Outline each blood parasite and name the species.
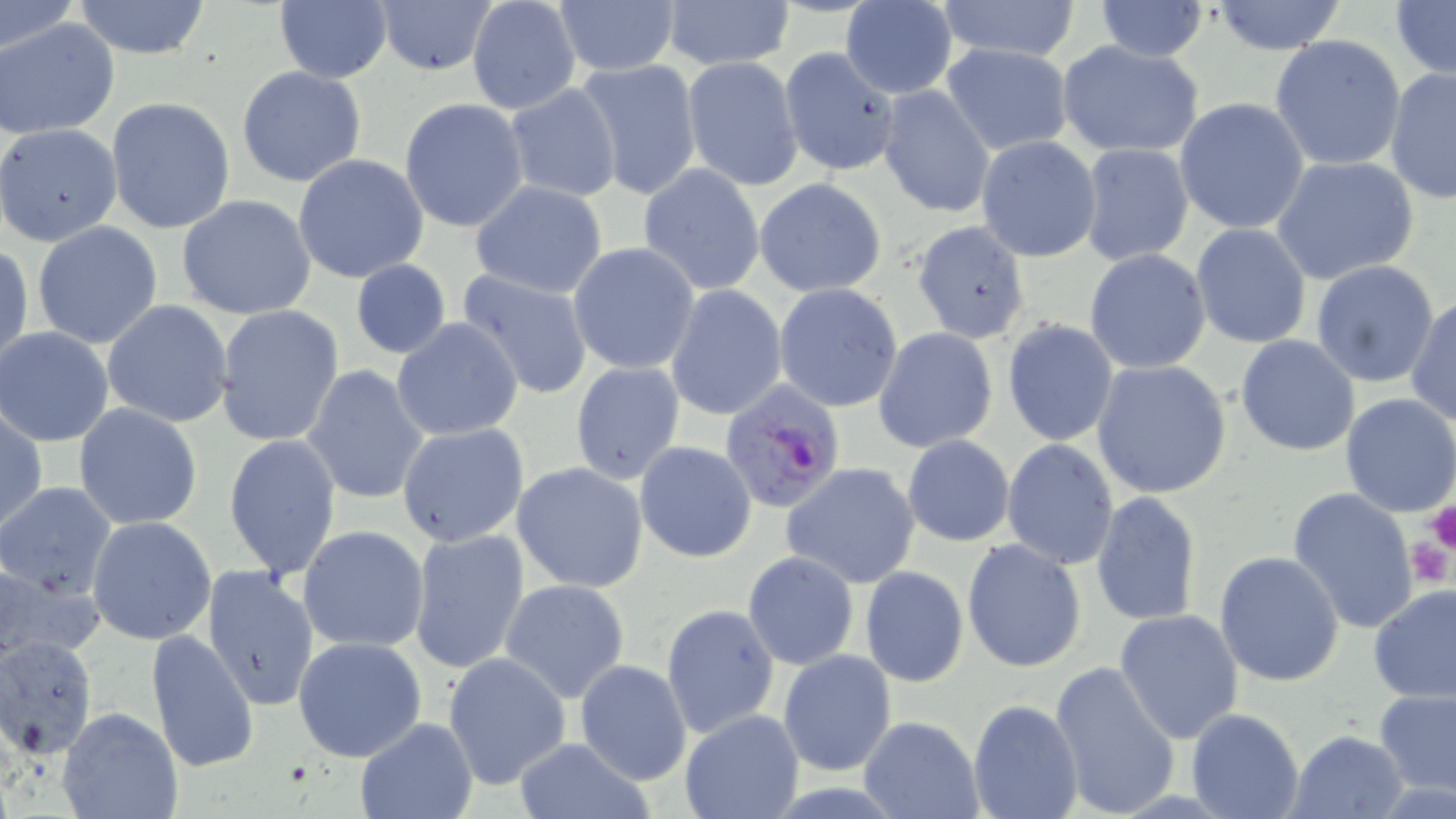
Approximate bounding boxes as named x1/y1/x2/y2 corners in pixels.
Plasmodium falciparum-infected red blood cells: (x1=718, y1=382, x2=846, y2=515).
No Plasmodium ovale, Plasmodium malariae, Plasmodium vivax, Babesia divergens, or Trypanosoma brucei observed.

Uninfected red blood cell locations: (x1=0, y1=0, x2=77, y2=57), (x1=70, y1=0, x2=214, y2=59), (x1=374, y1=0, x2=498, y2=75), (x1=466, y1=0, x2=582, y2=116), (x1=1093, y1=0, x2=1211, y2=62), (x1=273, y1=1, x2=392, y2=84), (x1=550, y1=1, x2=681, y2=76), (x1=658, y1=1, x2=797, y2=71), (x1=840, y1=1, x2=958, y2=98), (x1=933, y1=1, x2=1086, y2=65), (x1=1208, y1=1, x2=1349, y2=54), (x1=1391, y1=2, x2=1455, y2=82), (x1=2, y1=18, x2=121, y2=139), (x1=1269, y1=35, x2=1408, y2=173), (x1=1057, y1=41, x2=1205, y2=158), (x1=941, y1=43, x2=1074, y2=155), (x1=777, y1=46, x2=902, y2=177), (x1=681, y1=57, x2=804, y2=192), (x1=575, y1=58, x2=703, y2=200), (x1=236, y1=65, x2=367, y2=187), (x1=1384, y1=66, x2=1456, y2=203), (x1=504, y1=84, x2=623, y2=202), (x1=876, y1=86, x2=996, y2=218), (x1=106, y1=97, x2=236, y2=234), (x1=400, y1=97, x2=529, y2=233), (x1=1174, y1=97, x2=1310, y2=235), (x1=1, y1=125, x2=123, y2=247), (x1=976, y1=136, x2=1103, y2=262), (x1=1078, y1=143, x2=1196, y2=266), (x1=293, y1=154, x2=430, y2=284), (x1=1272, y1=156, x2=1421, y2=287), (x1=638, y1=164, x2=767, y2=294), (x1=754, y1=178, x2=888, y2=297), (x1=470, y1=181, x2=607, y2=298), (x1=176, y1=195, x2=318, y2=320), (x1=911, y1=219, x2=1031, y2=345), (x1=32, y1=222, x2=164, y2=350), (x1=1189, y1=223, x2=1313, y2=349), (x1=1, y1=241, x2=31, y2=372), (x1=569, y1=242, x2=700, y2=375), (x1=1085, y1=249, x2=1213, y2=374), (x1=349, y1=260, x2=451, y2=359), (x1=1311, y1=261, x2=1440, y2=387), (x1=457, y1=270, x2=594, y2=400), (x1=773, y1=283, x2=904, y2=413), (x1=663, y1=285, x2=789, y2=421), (x1=1406, y1=295, x2=1455, y2=427), (x1=102, y1=299, x2=235, y2=428), (x1=214, y1=304, x2=345, y2=448), (x1=391, y1=318, x2=523, y2=441), (x1=1002, y1=319, x2=1119, y2=446), (x1=0, y1=327, x2=113, y2=447), (x1=873, y1=328, x2=1000, y2=451), (x1=1235, y1=335, x2=1360, y2=457), (x1=1091, y1=360, x2=1233, y2=499), (x1=569, y1=362, x2=685, y2=486), (x1=303, y1=364, x2=430, y2=508), (x1=1338, y1=392, x2=1456, y2=518), (x1=73, y1=403, x2=203, y2=532), (x1=0, y1=408, x2=47, y2=535), (x1=396, y1=423, x2=530, y2=548), (x1=223, y1=434, x2=341, y2=579), (x1=901, y1=434, x2=1016, y2=547), (x1=1002, y1=438, x2=1119, y2=572), (x1=634, y1=441, x2=757, y2=562), (x1=512, y1=462, x2=650, y2=594), (x1=781, y1=462, x2=922, y2=590), (x1=0, y1=481, x2=116, y2=598), (x1=1287, y1=487, x2=1421, y2=635), (x1=1090, y1=492, x2=1202, y2=625), (x1=86, y1=516, x2=217, y2=644), (x1=297, y1=525, x2=429, y2=652), (x1=408, y1=528, x2=530, y2=674), (x1=961, y1=538, x2=1088, y2=673), (x1=742, y1=550, x2=859, y2=671), (x1=1214, y1=552, x2=1345, y2=687), (x1=1, y1=558, x2=102, y2=662), (x1=200, y1=563, x2=320, y2=712), (x1=860, y1=565, x2=969, y2=687), (x1=500, y1=578, x2=632, y2=703), (x1=1368, y1=583, x2=1456, y2=704), (x1=660, y1=603, x2=780, y2=738), (x1=1114, y1=609, x2=1244, y2=744), (x1=147, y1=629, x2=259, y2=774), (x1=293, y1=635, x2=426, y2=762), (x1=0, y1=636, x2=98, y2=758), (x1=777, y1=649, x2=896, y2=777), (x1=442, y1=651, x2=571, y2=791), (x1=1050, y1=659, x2=1180, y2=817), (x1=573, y1=660, x2=692, y2=785), (x1=1373, y1=688, x2=1456, y2=798), (x1=968, y1=699, x2=1083, y2=818), (x1=58, y1=706, x2=182, y2=819), (x1=1186, y1=707, x2=1305, y2=819), (x1=679, y1=711, x2=803, y2=819), (x1=858, y1=715, x2=983, y2=818), (x1=354, y1=716, x2=475, y2=819), (x1=1286, y1=729, x2=1409, y2=818), (x1=513, y1=737, x2=656, y2=819). Platelet locations: (x1=1426, y1=500, x2=1456, y2=554), (x1=1405, y1=538, x2=1454, y2=589). Slide-level diagnosis: Plasmodium falciparum. 1000x magnification. May-Grünwald-Giemsa-stained preparation. Single field of view. Light microscopy. Image is 1456×819 pixels. Thin blood smear.